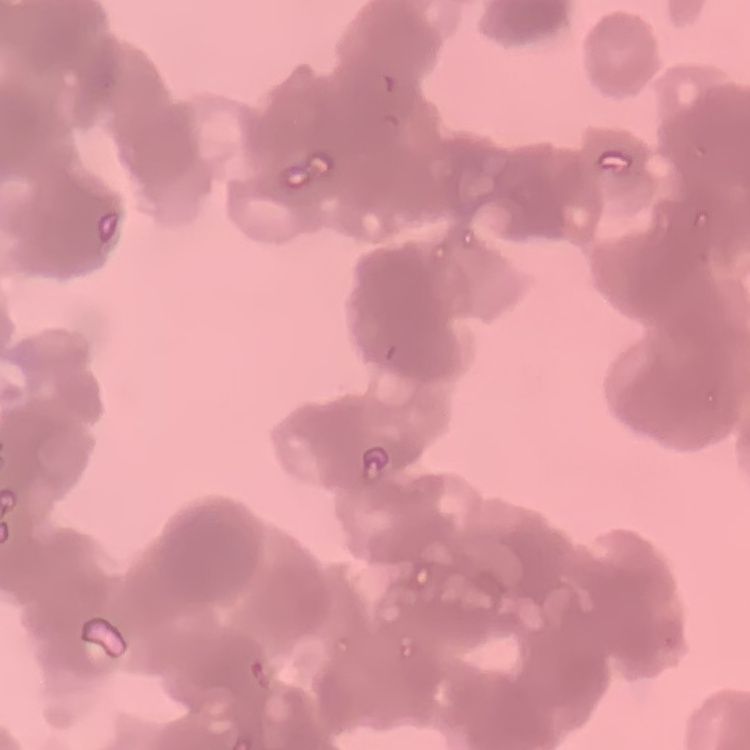
Summary:
  - Red blood cell morphology: rouleaux formation
  - Preparation: thin peripheral smear
  - Stain: Field's or Giemsa
  - Image type: square crop of a larger photomicrograph